Assess this cell for malaria.
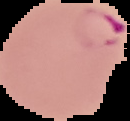
It is parasitized.

preparation = thin blood film
image size = 130×121 pixels
image type = segmented cell region with the area outside set to black